State the preparation type.
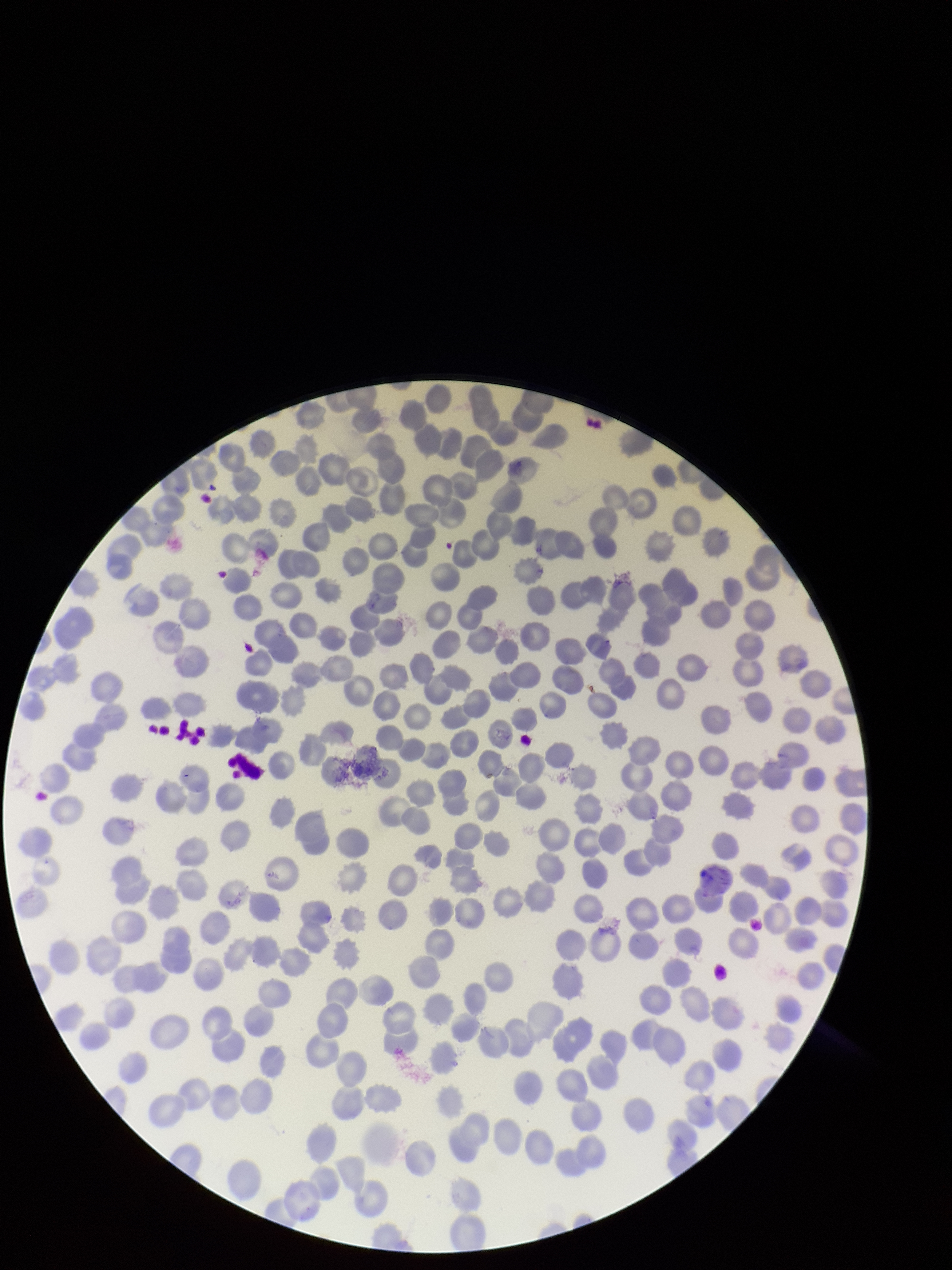

A thin smear.

Summary:
  - Red blood cell count: 241
  - Parasitized red blood cell count: 0
  - Patient malaria status: positive
  - Capture: smartphone photograph through the microscope eyepiece
  - Stain: Giemsa
  - Image size: 952×1270 pixels
  - Field of view: one from this slide
  - Parasitized red blood cells: none identified
  - Species reported for this patient: Plasmodium falciparum